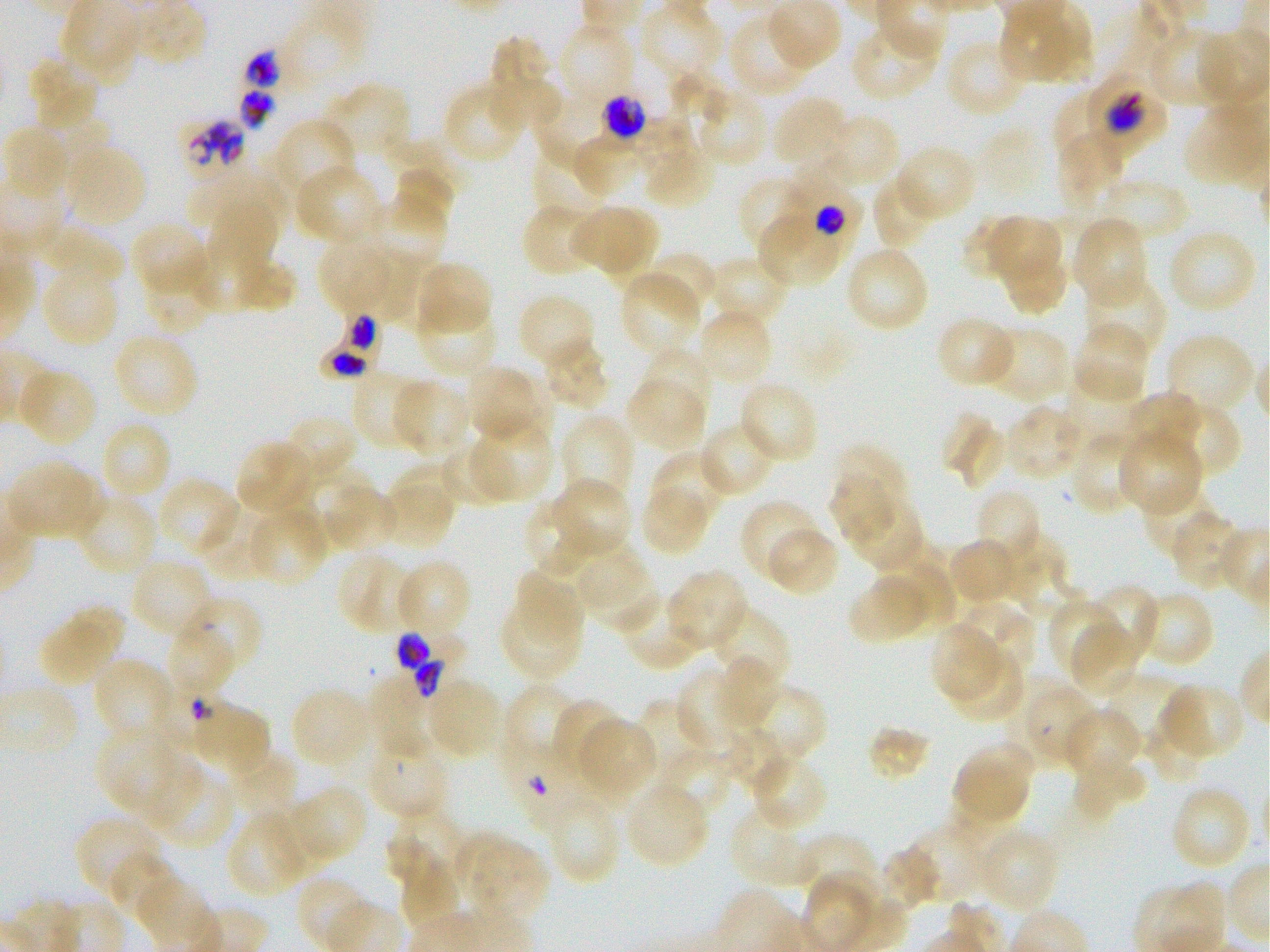
Not every red blood cell is marked. A life-cycle stage — or a range of stages, where the recorded stages span more than one — follows each staged infected red blood cell.
stain = Giemsa
locations of uninfected red blood cells = approximate bounding rectangles given as corner coordinates in pixels from the top-left: (x1=762, y1=0, x2=842, y2=73), (x1=999, y1=1, x2=1094, y2=86), (x1=641, y1=3, x2=728, y2=77), (x1=728, y1=13, x2=814, y2=99), (x1=275, y1=14, x2=368, y2=96), (x1=851, y1=19, x2=943, y2=101), (x1=555, y1=23, x2=634, y2=109), (x1=1148, y1=26, x2=1234, y2=107), (x1=1194, y1=29, x2=1270, y2=110), (x1=486, y1=36, x2=562, y2=128), (x1=946, y1=38, x2=1030, y2=119), (x1=27, y1=55, x2=100, y2=132), (x1=443, y1=81, x2=526, y2=166), (x1=319, y1=82, x2=412, y2=165), (x1=1054, y1=90, x2=1118, y2=157), (x1=701, y1=95, x2=766, y2=162), (x1=771, y1=95, x2=851, y2=174), (x1=821, y1=114, x2=900, y2=191), (x1=276, y1=119, x2=354, y2=193), (x1=1, y1=124, x2=73, y2=201), (x1=1054, y1=129, x2=1125, y2=209), (x1=532, y1=142, x2=611, y2=217), (x1=641, y1=142, x2=717, y2=209), (x1=63, y1=144, x2=148, y2=228), (x1=894, y1=144, x2=978, y2=224), (x1=391, y1=162, x2=456, y2=239), (x1=297, y1=167, x2=380, y2=243), (x1=193, y1=168, x2=290, y2=229), (x1=872, y1=172, x2=943, y2=250), (x1=1102, y1=172, x2=1193, y2=245), (x1=737, y1=173, x2=812, y2=256), (x1=358, y1=195, x2=448, y2=269), (x1=208, y1=197, x2=281, y2=274), (x1=521, y1=203, x2=600, y2=278), (x1=568, y1=203, x2=659, y2=281), (x1=977, y1=214, x2=1067, y2=308), (x1=1072, y1=216, x2=1148, y2=308), (x1=757, y1=218, x2=839, y2=283), (x1=130, y1=222, x2=210, y2=300), (x1=53, y1=228, x2=123, y2=284), (x1=1167, y1=229, x2=1257, y2=315), (x1=316, y1=237, x2=405, y2=318), (x1=843, y1=245, x2=930, y2=335), (x1=186, y1=246, x2=293, y2=315), (x1=375, y1=250, x2=427, y2=328), (x1=644, y1=252, x2=720, y2=324), (x1=708, y1=255, x2=792, y2=325), (x1=140, y1=257, x2=218, y2=333), (x1=413, y1=261, x2=494, y2=338), (x1=620, y1=269, x2=703, y2=358), (x1=1085, y1=273, x2=1166, y2=362), (x1=48, y1=280, x2=116, y2=343), (x1=415, y1=296, x2=496, y2=378), (x1=521, y1=298, x2=592, y2=369), (x1=695, y1=307, x2=774, y2=388), (x1=936, y1=316, x2=1017, y2=389), (x1=1072, y1=321, x2=1150, y2=406), (x1=977, y1=325, x2=1071, y2=403), (x1=112, y1=331, x2=199, y2=419), (x1=1163, y1=333, x2=1256, y2=417), (x1=542, y1=336, x2=611, y2=411), (x1=638, y1=347, x2=715, y2=420), (x1=464, y1=364, x2=547, y2=446), (x1=17, y1=366, x2=97, y2=448), (x1=350, y1=370, x2=430, y2=451), (x1=625, y1=372, x2=708, y2=452), (x1=1062, y1=374, x2=1145, y2=453), (x1=389, y1=378, x2=473, y2=459), (x1=738, y1=380, x2=820, y2=464), (x1=1120, y1=392, x2=1204, y2=465), (x1=1149, y1=399, x2=1242, y2=479), (x1=1004, y1=404, x2=1088, y2=480), (x1=281, y1=414, x2=357, y2=491), (x1=560, y1=414, x2=635, y2=505), (x1=943, y1=414, x2=1006, y2=490), (x1=469, y1=419, x2=555, y2=502), (x1=98, y1=420, x2=171, y2=502), (x1=697, y1=422, x2=776, y2=499), (x1=1115, y1=429, x2=1204, y2=517), (x1=1069, y1=430, x2=1147, y2=516), (x1=235, y1=440, x2=317, y2=519), (x1=440, y1=440, x2=520, y2=509), (x1=830, y1=445, x2=911, y2=545), (x1=649, y1=450, x2=727, y2=529), (x1=6, y1=458, x2=103, y2=542), (x1=393, y1=463, x2=461, y2=513), (x1=155, y1=476, x2=240, y2=558), (x1=549, y1=478, x2=632, y2=560), (x1=320, y1=482, x2=398, y2=556), (x1=638, y1=483, x2=713, y2=556), (x1=1140, y1=485, x2=1220, y2=558), (x1=380, y1=486, x2=453, y2=540), (x1=840, y1=489, x2=925, y2=574), (x1=973, y1=489, x2=1041, y2=567), (x1=75, y1=494, x2=159, y2=576), (x1=525, y1=499, x2=603, y2=575), (x1=740, y1=501, x2=823, y2=583), (x1=248, y1=505, x2=330, y2=587), (x1=202, y1=509, x2=275, y2=575), (x1=1170, y1=509, x2=1246, y2=590), (x1=764, y1=525, x2=840, y2=597), (x1=989, y1=534, x2=1068, y2=610), (x1=947, y1=538, x2=1021, y2=608), (x1=877, y1=547, x2=957, y2=634), (x1=337, y1=551, x2=421, y2=635), (x1=582, y1=554, x2=658, y2=631), (x1=128, y1=557, x2=215, y2=641), (x1=393, y1=558, x2=473, y2=642), (x1=511, y1=559, x2=604, y2=654), (x1=667, y1=569, x2=748, y2=652), (x1=847, y1=571, x2=936, y2=645), (x1=1087, y1=584, x2=1160, y2=669), (x1=499, y1=589, x2=584, y2=681), (x1=1136, y1=589, x2=1215, y2=669), (x1=618, y1=591, x2=704, y2=670), (x1=1047, y1=597, x2=1124, y2=680), (x1=192, y1=598, x2=260, y2=668), (x1=952, y1=600, x2=1036, y2=682), (x1=37, y1=602, x2=125, y2=688), (x1=708, y1=604, x2=791, y2=691), (x1=1070, y1=620, x2=1144, y2=700), (x1=932, y1=624, x2=1000, y2=700), (x1=168, y1=625, x2=235, y2=690), (x1=953, y1=647, x2=1025, y2=722), (x1=95, y1=658, x2=177, y2=734), (x1=715, y1=659, x2=780, y2=730), (x1=678, y1=666, x2=760, y2=759), (x1=368, y1=671, x2=446, y2=757), (x1=424, y1=677, x2=504, y2=761), (x1=1011, y1=680, x2=1099, y2=771), (x1=501, y1=681, x2=580, y2=771), (x1=1156, y1=683, x2=1246, y2=762), (x1=736, y1=684, x2=826, y2=771), (x1=290, y1=687, x2=375, y2=771), (x1=634, y1=697, x2=709, y2=785), (x1=551, y1=699, x2=626, y2=782), (x1=1061, y1=707, x2=1144, y2=785), (x1=574, y1=716, x2=658, y2=805), (x1=1146, y1=718, x2=1209, y2=785), (x1=869, y1=726, x2=931, y2=781), (x1=97, y1=728, x2=173, y2=804), (x1=722, y1=728, x2=794, y2=794), (x1=364, y1=732, x2=448, y2=822), (x1=951, y1=741, x2=1034, y2=830), (x1=661, y1=751, x2=732, y2=807), (x1=231, y1=752, x2=297, y2=818), (x1=748, y1=752, x2=828, y2=833), (x1=1070, y1=753, x2=1148, y2=821), (x1=145, y1=760, x2=202, y2=828), (x1=159, y1=774, x2=236, y2=846), (x1=622, y1=781, x2=709, y2=869), (x1=1169, y1=784, x2=1253, y2=871), (x1=284, y1=785, x2=366, y2=868), (x1=546, y1=794, x2=623, y2=885), (x1=730, y1=805, x2=818, y2=890), (x1=228, y1=807, x2=319, y2=896), (x1=386, y1=809, x2=469, y2=892), (x1=75, y1=814, x2=165, y2=901), (x1=906, y1=818, x2=992, y2=904), (x1=975, y1=828, x2=1060, y2=913), (x1=454, y1=829, x2=548, y2=923), (x1=794, y1=832, x2=879, y2=905), (x1=884, y1=842, x2=943, y2=906), (x1=103, y1=852, x2=180, y2=928), (x1=801, y1=863, x2=892, y2=952)
locations of infected red blood cells = approximate bounding rectangles given as corner coordinates in pixels from the top-left: (x1=1081, y1=68, x2=1167, y2=159) trophozoite; (x1=588, y1=73, x2=665, y2=155) late trophozoite to early schizont; (x1=164, y1=110, x2=252, y2=186); (x1=771, y1=162, x2=866, y2=247) early trophozoite; (x1=321, y1=311, x2=379, y2=378); (x1=395, y1=619, x2=474, y2=703)
image size = 1270×952 pixels
preparation = thin blood smear
objective = 100x, oil immersion, numerical aperture 1.25
culture = Plasmodium falciparum strain 3D7, static, in vitro
locations of red blood cells of indeterminate infection status = approximate bounding rectangles given as corner coordinates in pixels from the top-left: (x1=240, y1=43, x2=283, y2=93), (x1=236, y1=85, x2=279, y2=134), (x1=497, y1=734, x2=585, y2=831)
donor blood group = O+
field of view = single